State which cell type is depicted.
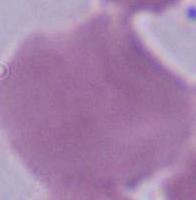

An erythrocyte.

{
  "modality": "micrograph",
  "magnification": "1000x"
}